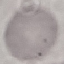
{
  "malaria_status": "uninfected",
  "preparation": "thin smear",
  "stain": "Giemsa",
  "capture": "smartphone through the microscope eyepiece",
  "image_type": "cell patch, automatically extracted from a larger field of view and resized to 64 × 64 pixels"
}